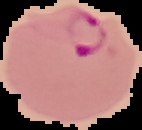 Malaria status: parasitized. From a thin blood film. The area outside the segmented cell region is set to black. Image is 142×130 pixels.